Identify the parasite.
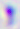

This is Toxoplasma gondii.

magnification = 400x
modality = photomicrograph